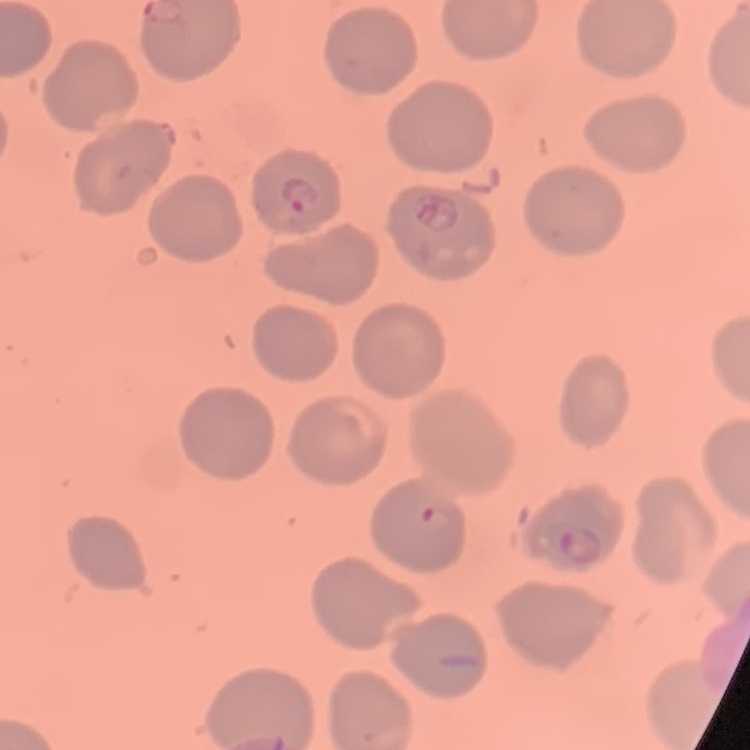

red_blood_cell_morphology: no rouleaux formation
stain: Field's or Giemsa
preparation: thin blood film
image_type: square crop of a larger photomicrograph